Locate every Plasmodium falciparum-infected red blood cell.
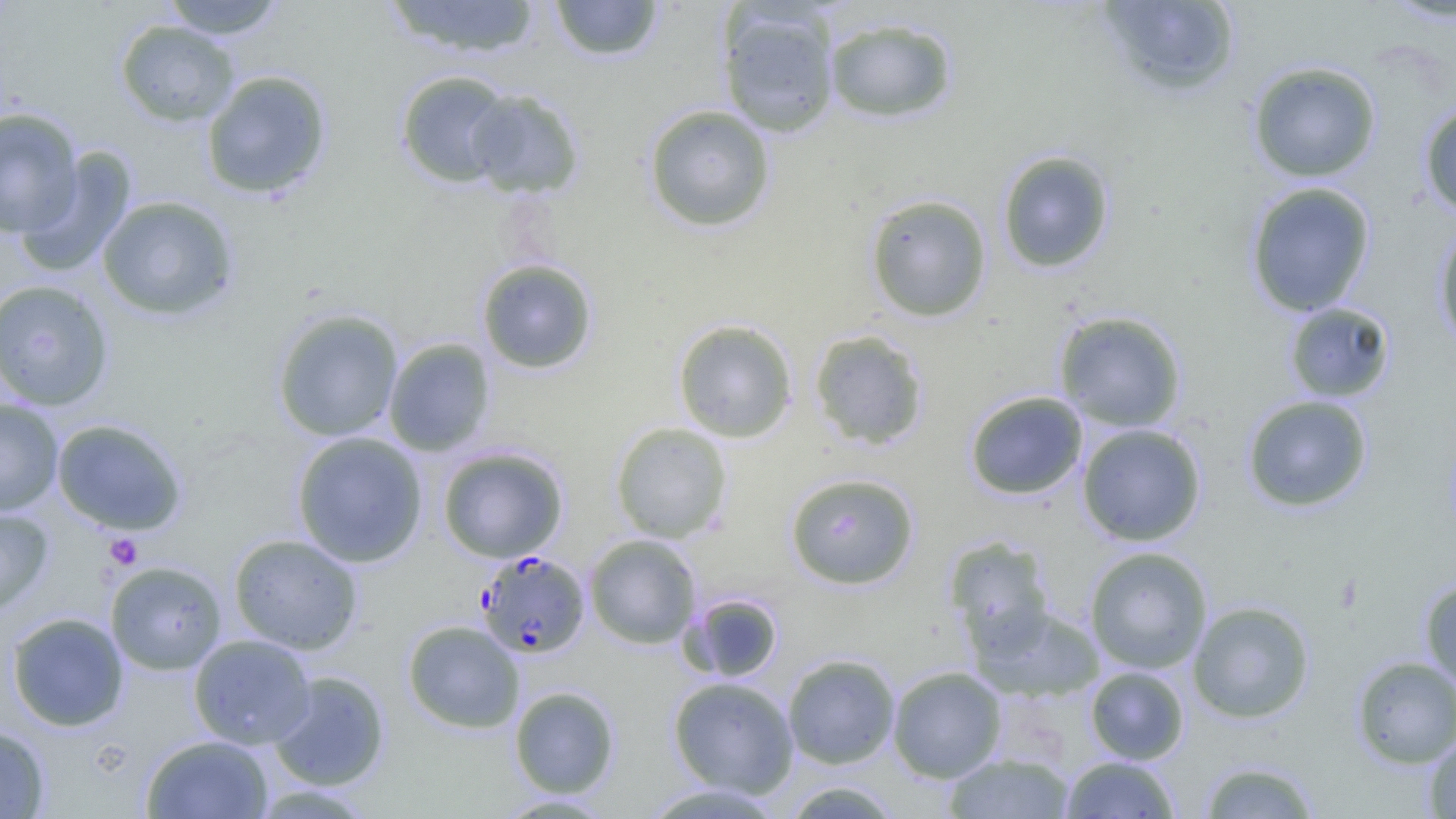

Approximate bounding boxes as [x1, y1, x2, y2] in pixels.
Plasmodium falciparum-infected red blood cells: [476, 550, 591, 658].

Summary:
  - Platelet locations: [104, 533, 143, 570]
  - Uninfected red blood cell locations: [160, 0, 289, 39], [385, 0, 542, 59], [549, 0, 665, 62], [1381, 0, 1456, 25], [1097, 1, 1243, 98], [717, 5, 841, 137], [824, 16, 958, 123], [115, 20, 240, 126], [1248, 61, 1382, 182], [201, 69, 332, 199], [395, 70, 514, 188], [464, 89, 584, 198], [1419, 101, 1456, 219], [643, 104, 776, 232], [0, 108, 83, 237], [16, 147, 138, 278], [997, 150, 1115, 273], [1245, 182, 1376, 317], [864, 193, 992, 322], [97, 195, 239, 322], [1433, 220, 1456, 351], [476, 259, 598, 373], [0, 279, 115, 411], [1284, 302, 1396, 403], [271, 308, 404, 442], [1053, 310, 1187, 432], [672, 319, 798, 443], [809, 329, 929, 450], [384, 338, 496, 456], [964, 391, 1088, 500], [1241, 395, 1373, 513], [0, 399, 63, 516], [52, 418, 188, 535], [611, 422, 732, 543], [1077, 423, 1207, 546], [291, 431, 428, 567], [438, 446, 568, 563], [785, 472, 920, 589], [0, 506, 54, 618], [228, 533, 363, 655], [585, 535, 701, 648], [944, 537, 1056, 656], [1084, 546, 1213, 674], [105, 560, 227, 675], [1419, 578, 1456, 693], [683, 593, 783, 682], [1187, 600, 1316, 724], [975, 605, 1104, 702], [7, 612, 129, 731], [402, 619, 524, 733], [188, 634, 316, 749], [782, 654, 900, 768], [1351, 656, 1456, 768], [888, 666, 1007, 782], [1085, 666, 1189, 764], [268, 671, 389, 791], [668, 676, 798, 797], [509, 686, 620, 798], [0, 724, 50, 818], [141, 734, 273, 818], [1423, 736, 1456, 819], [943, 752, 1075, 818], [1061, 755, 1181, 818], [1198, 759, 1322, 818], [780, 780, 906, 818], [638, 783, 787, 818], [494, 793, 618, 817]
  - Slide-level diagnosis: Plasmodium falciparum
  - Field of view: one of a larger specimen
  - Modality: optical microscopy
  - Image size: 1456×819 pixels
  - Preparation: thin blood smear
  - Magnification: 1000x